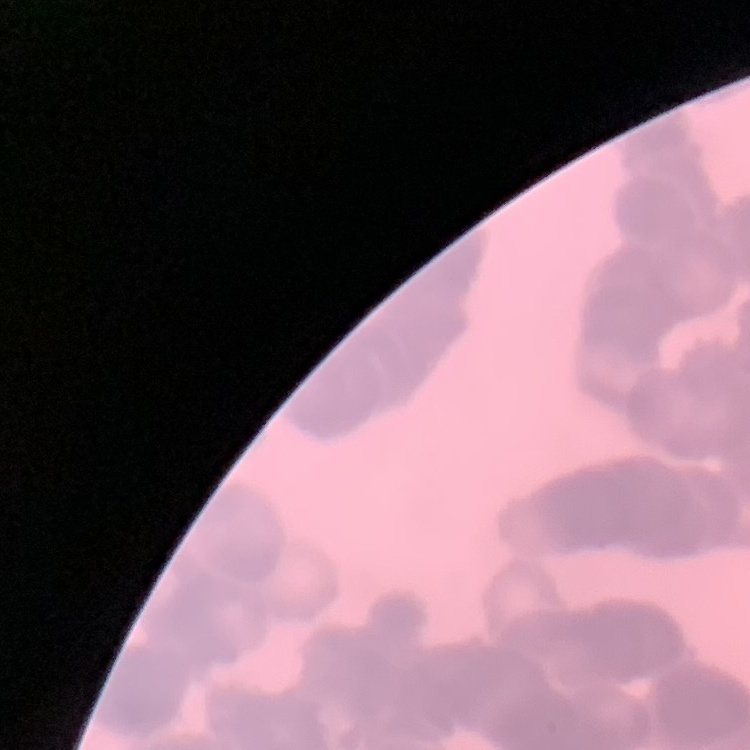

erythrocyte morphology = rouleaux formation
stain = Field's or Giemsa
image type = square crop of a larger photomicrograph
preparation = thin blood film